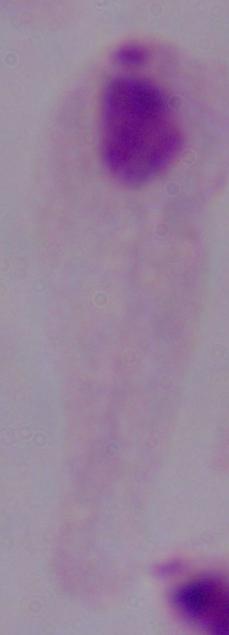
Summary:
  - Identification: trichomonad
  - Magnification: 1000x
  - Modality: micrograph